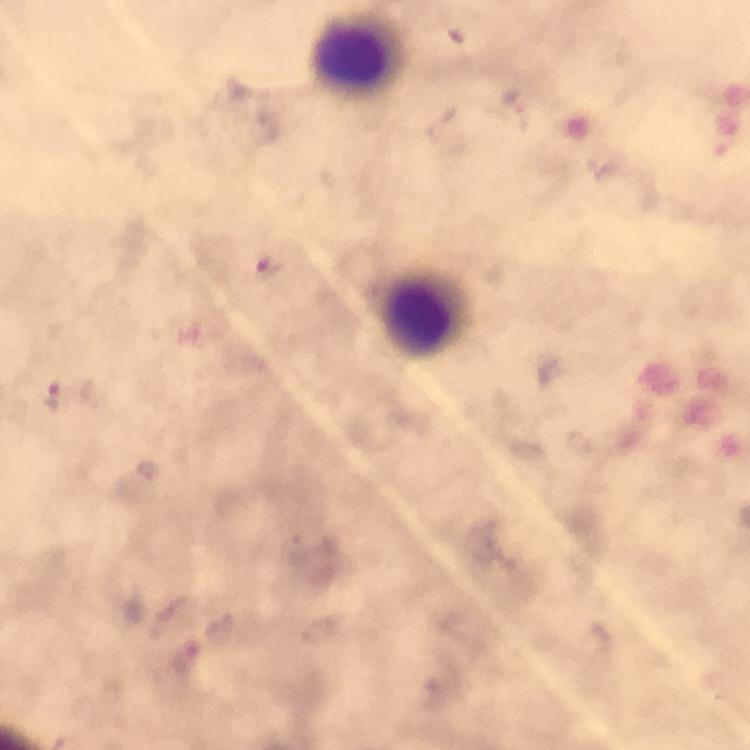
Approximate centers as {x, y} in pixels.
Summary:
  - Leukocyte locations: {353, 55}, {421, 315}
  - Preparation: thick smear
  - Image size: 750×750 pixels
  - Context: from a malaria diagnostic workup
  - Stain: Giemsa
  - Cropped from: a single field of view
  - Immersion oil: used
  - Plasmodium parasites: none seen
  - Magnification: 100x
  - Capture: smartphone photograph through a microscope